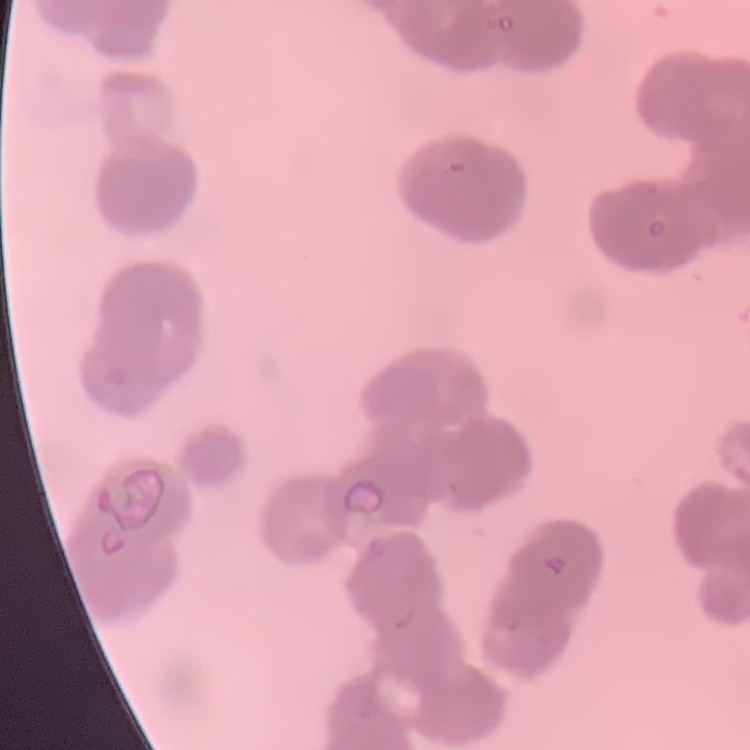

Summary:
  - Red blood cell morphology: rouleaux formation
  - Image type: one tile cut from a larger photomicrograph
  - Stain: Field's or Giemsa
  - Preparation: thin blood film